Name the parasite shown.
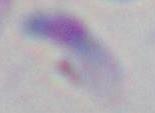
Toxoplasma gondii.

Photomicrograph. 1000x magnification.